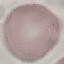
Summary:
  - Malaria status: uninfected
  - Stain: Giemsa
  - Preparation: thin smear
  - Capture: smartphone through the microscope eyepiece
  - Image type: automatically extracted cell patch, resized to 64 × 64 pixels